Outline each blood parasite and name the species.
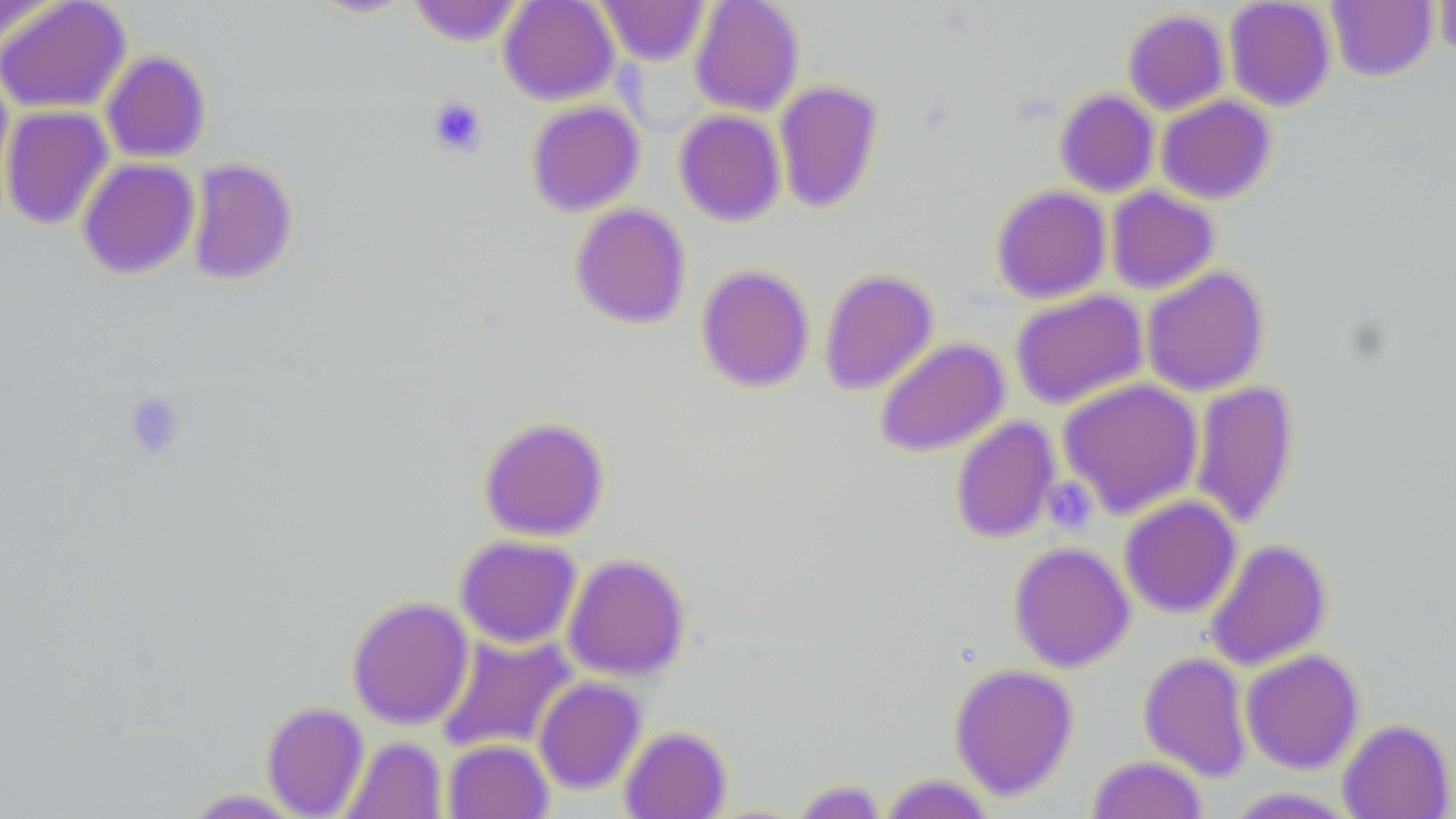
No blood parasites observed.

Approximate bounding boxes as [x1, y1, x2, y2] in pixels. Uninfected red blood cell locations: [0, 0, 131, 114], [307, 0, 414, 18], [498, 0, 619, 105], [689, 0, 805, 117], [1223, 0, 1336, 111], [0, 1, 64, 50], [408, 1, 525, 46], [596, 1, 709, 66], [1326, 1, 1437, 82], [1432, 1, 1456, 61], [1122, 9, 1229, 116], [100, 49, 211, 163], [614, 50, 713, 138], [0, 66, 15, 215], [773, 80, 884, 214], [1054, 89, 1160, 198], [1156, 96, 1276, 204], [525, 101, 645, 217], [0, 105, 114, 231], [673, 109, 786, 226], [185, 157, 298, 286], [77, 158, 200, 280], [991, 185, 1111, 303], [1105, 186, 1219, 294], [569, 203, 691, 330], [696, 264, 815, 393], [1141, 266, 1270, 397], [819, 268, 939, 396], [1010, 289, 1148, 410], [874, 337, 1009, 457], [1057, 377, 1204, 519], [1189, 380, 1300, 530], [478, 416, 609, 542], [949, 416, 1061, 543], [1118, 496, 1241, 619], [454, 535, 582, 648], [1204, 538, 1331, 672], [1008, 541, 1135, 672], [562, 553, 690, 681], [346, 596, 474, 730], [434, 632, 579, 755], [1240, 649, 1364, 773], [1139, 651, 1252, 781], [949, 664, 1079, 800], [533, 676, 647, 794], [261, 701, 369, 817], [1337, 718, 1454, 818], [619, 726, 731, 819], [338, 736, 447, 819], [442, 739, 554, 819], [1086, 755, 1208, 818], [878, 774, 996, 818], [793, 779, 886, 818], [1221, 787, 1360, 818], [177, 788, 309, 818]. Platelet locations: [427, 96, 487, 157], [122, 390, 187, 459], [1042, 476, 1098, 535]. Slide-level diagnosis: negative for blood parasites. Captured at 1000x magnification. Thin blood smear. May-Grünwald-Giemsa stain. Image is 1456×819 pixels. Light microscopy. One field of a larger specimen.